Classify this cell by malaria status.
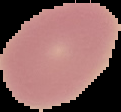

It is uninfected.

Summary:
  - Image size: 121×112 pixels
  - Image type: segmented cell region on a black background
  - Preparation: thin blood smear